State which parasite is depicted.
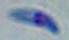
This is Toxoplasma gondii.

Summary:
  - Modality: micrograph
  - Magnification: 1000x